Outline each blood parasite and name the species.
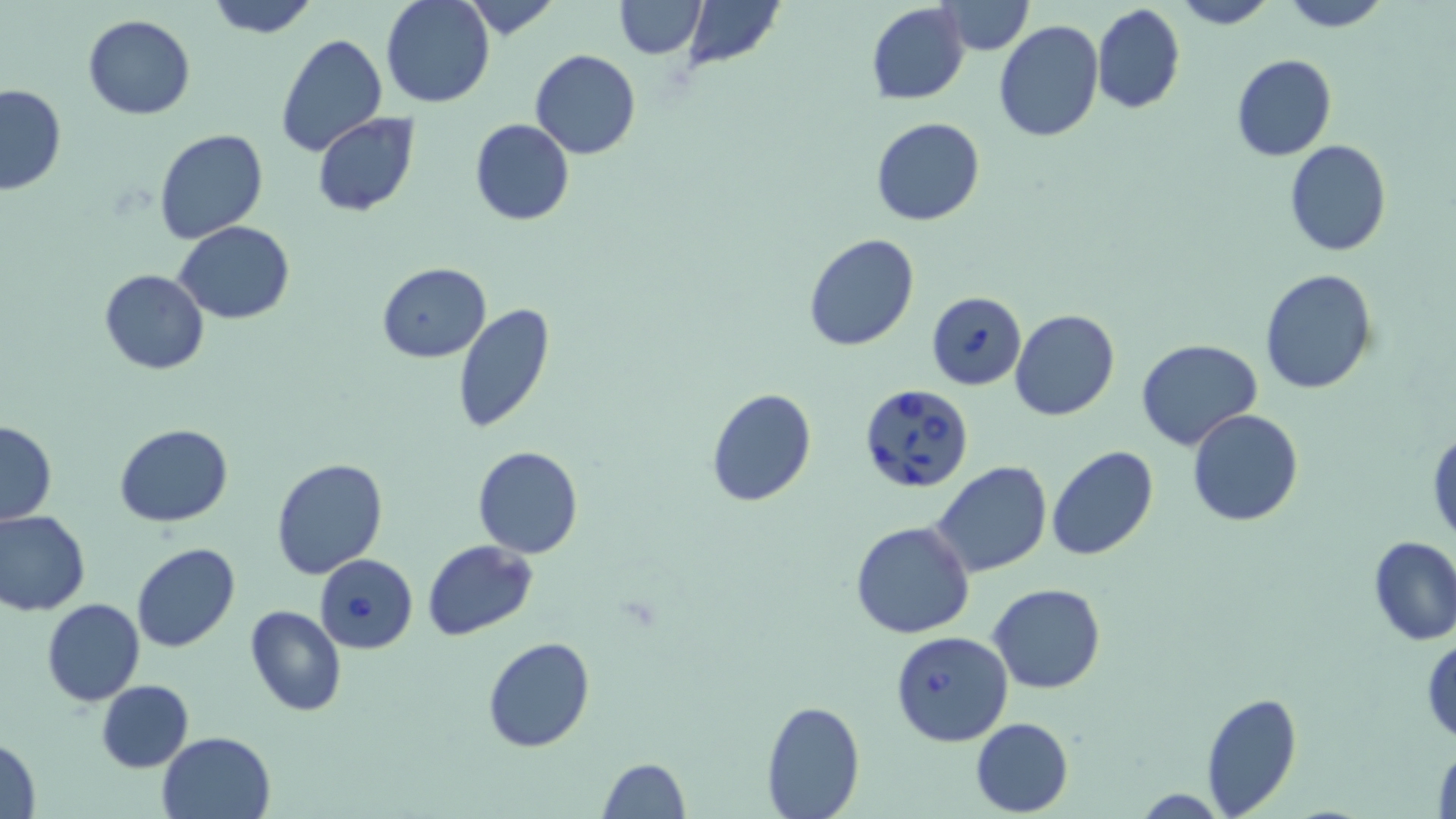
Approximate bounding boxes as (x1, y1, x2, y2) in pixels.
Babesia divergens-infected red blood cells: (926, 290, 1026, 390), (858, 382, 976, 493), (314, 553, 417, 653), (890, 630, 1013, 747).
No Plasmodium falciparum, Plasmodium ovale, Plasmodium malariae, Plasmodium vivax, or Trypanosoma brucei observed.

Uninfected red blood cell locations: (204, 0, 320, 39), (381, 0, 493, 108), (461, 0, 560, 40), (613, 0, 705, 57), (683, 0, 784, 69), (1169, 0, 1276, 28), (1276, 0, 1393, 31), (939, 1, 1032, 55), (866, 2, 969, 105), (1092, 2, 1187, 115), (83, 15, 196, 119), (993, 20, 1104, 141), (276, 32, 387, 158), (530, 50, 640, 159), (1231, 54, 1337, 161), (0, 84, 67, 195), (312, 113, 420, 217), (871, 117, 985, 227), (470, 119, 574, 226), (154, 127, 268, 245), (1284, 139, 1391, 256), (174, 219, 294, 324), (802, 232, 920, 350), (376, 263, 491, 363), (100, 269, 208, 374), (1259, 269, 1378, 395), (452, 304, 555, 433), (1009, 309, 1120, 421), (1136, 338, 1263, 451), (705, 388, 816, 508), (1188, 410, 1304, 527), (1, 420, 58, 526), (114, 423, 233, 527), (1428, 428, 1456, 551), (472, 445, 584, 559), (1046, 446, 1160, 563), (269, 458, 388, 581), (932, 462, 1053, 579), (0, 508, 91, 616), (850, 521, 975, 639), (1367, 536, 1456, 647), (422, 540, 538, 640), (132, 541, 241, 653), (989, 582, 1106, 694), (41, 598, 146, 706), (245, 604, 347, 716), (483, 636, 594, 753), (1423, 636, 1455, 743), (96, 679, 194, 773), (1201, 691, 1303, 817), (760, 699, 863, 818), (970, 717, 1073, 816), (156, 730, 275, 819), (0, 736, 43, 817), (1431, 744, 1455, 818), (598, 759, 688, 818). Slide-level diagnosis: Babesia divergens. May-Grünwald-Giemsa stain. Image is 1456×819 pixels. Thin blood smear. One field of a larger specimen. Light microscopy. 1000x magnification.